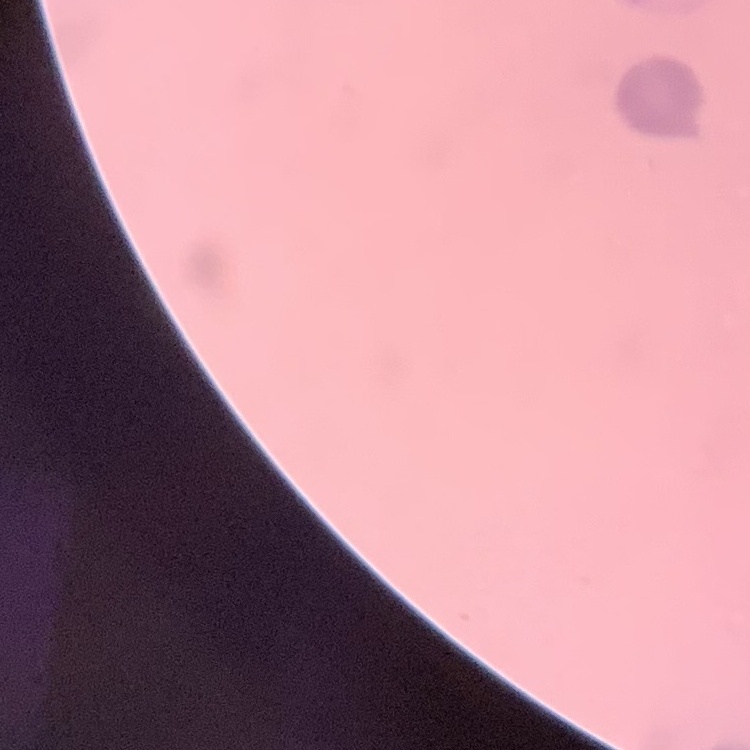

erythrocyte morphology = rouleaux formation
preparation = thin peripheral smear
image type = one tile cut from a larger photomicrograph
stain = Field's or Giemsa